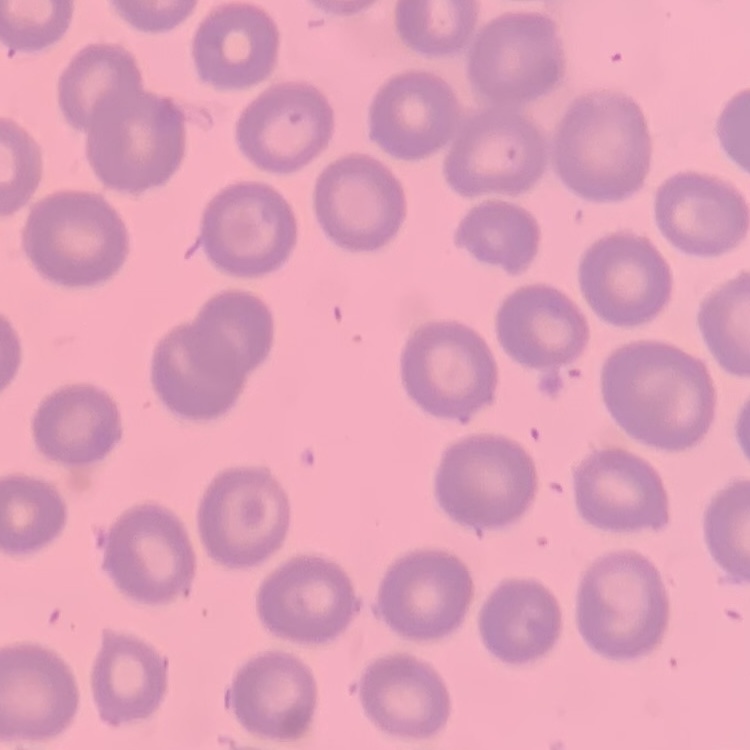
Summary:
  - Red blood cell morphology: no rouleaux formation
  - Preparation: thin blood film
  - Stain: Field's or Giemsa
  - Image type: square crop of a larger photomicrograph